Identify the blood parasite species.
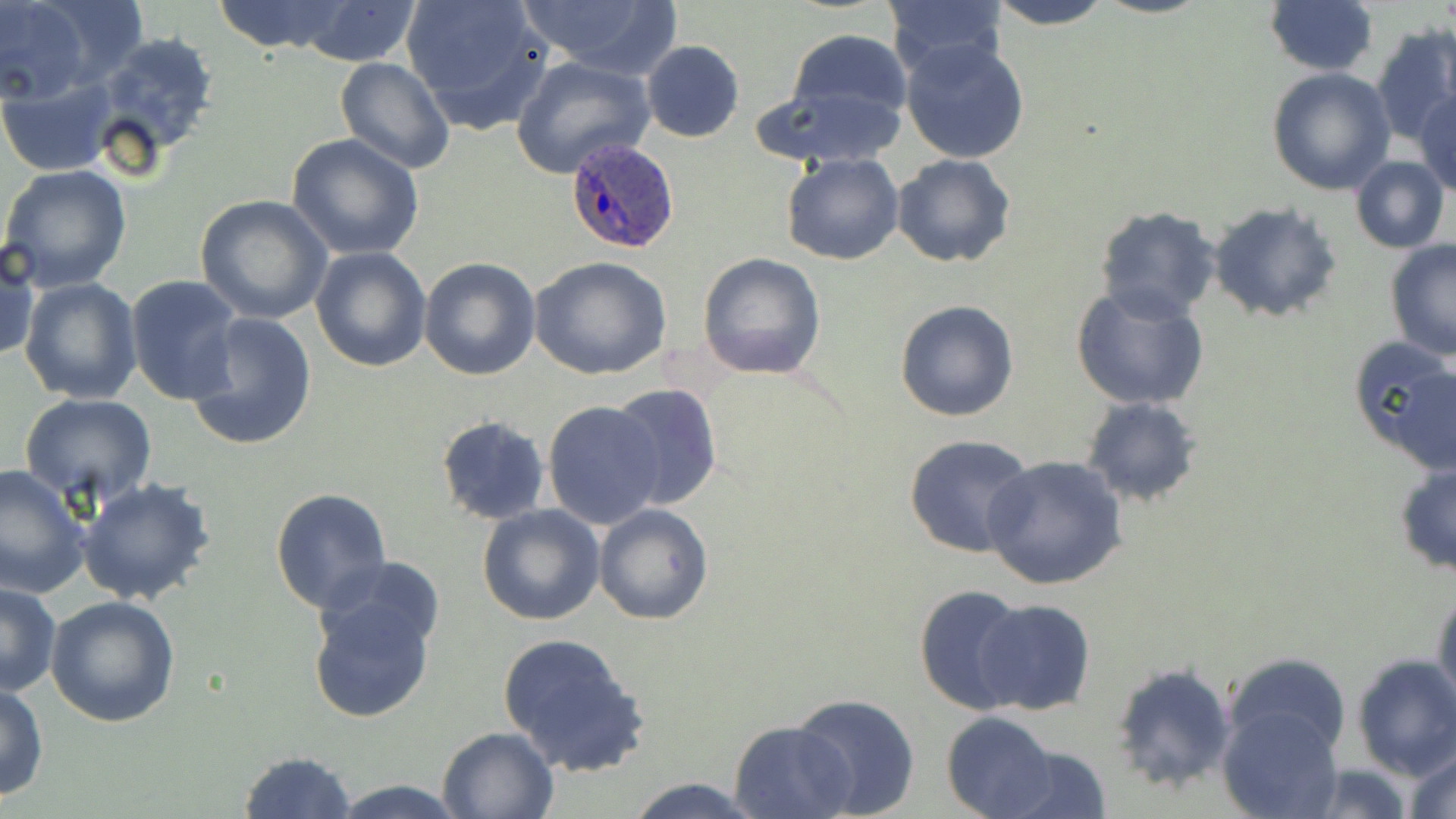

Plasmodium ovale.

Summary:
  - Coordinate format: approximate bounding boxes as [x1, y1, x2, y2] in pixels
  - Uninfected red blood cell locations: [0, 0, 90, 104], [210, 0, 352, 53], [292, 0, 423, 66], [402, 0, 554, 131], [519, 0, 680, 76], [881, 0, 1010, 77], [986, 0, 1118, 29], [1264, 1, 1379, 77], [1369, 23, 1456, 145], [783, 29, 913, 129], [88, 30, 222, 162], [900, 38, 1031, 165], [640, 40, 746, 142], [511, 53, 655, 178], [334, 55, 455, 174], [1268, 66, 1397, 194], [0, 80, 116, 176], [752, 85, 908, 168], [1414, 89, 1456, 196], [285, 132, 425, 262], [782, 152, 904, 266], [892, 154, 1016, 269], [1348, 156, 1450, 254], [0, 164, 132, 293], [194, 193, 333, 324], [1206, 200, 1343, 326], [1094, 206, 1223, 322], [1, 238, 39, 365], [1384, 238, 1456, 361], [310, 247, 431, 372], [697, 252, 826, 379], [529, 255, 672, 380], [420, 256, 540, 381], [125, 274, 245, 405], [20, 278, 143, 405], [1070, 284, 1209, 411], [896, 300, 1019, 421], [183, 310, 317, 451], [1346, 338, 1456, 464], [608, 381, 724, 510], [17, 393, 158, 508], [1080, 397, 1201, 506], [542, 401, 665, 529], [435, 417, 551, 525], [903, 434, 1034, 558], [982, 454, 1131, 592], [1393, 461, 1456, 579], [0, 465, 90, 598], [76, 478, 218, 608], [270, 488, 393, 613], [593, 503, 713, 624], [477, 506, 605, 625], [311, 554, 447, 661], [1, 581, 61, 697], [306, 582, 441, 725], [1432, 583, 1456, 714], [913, 585, 1031, 716], [45, 594, 182, 726], [973, 600, 1096, 716], [497, 631, 649, 776], [1223, 651, 1351, 763], [1351, 655, 1456, 780], [1111, 661, 1236, 792], [0, 683, 49, 801], [793, 692, 920, 816], [1217, 705, 1345, 819], [939, 713, 1060, 819], [729, 719, 854, 819], [436, 725, 558, 817], [995, 740, 1116, 819], [1405, 742, 1456, 819], [236, 750, 358, 819], [1301, 763, 1418, 819], [624, 775, 763, 818], [329, 777, 465, 817]
  - Plasmodium ovale-infected red blood cell locations: [565, 137, 681, 255]
  - Magnification: 1000x
  - Image size: 1456×819 pixels
  - Modality: light microscopy
  - Field of view: one of a larger specimen
  - Stain: May-Grünwald-Giemsa
  - Preparation: thin blood smear